Locate every Plasmodium falciparum-infected red blood cell.
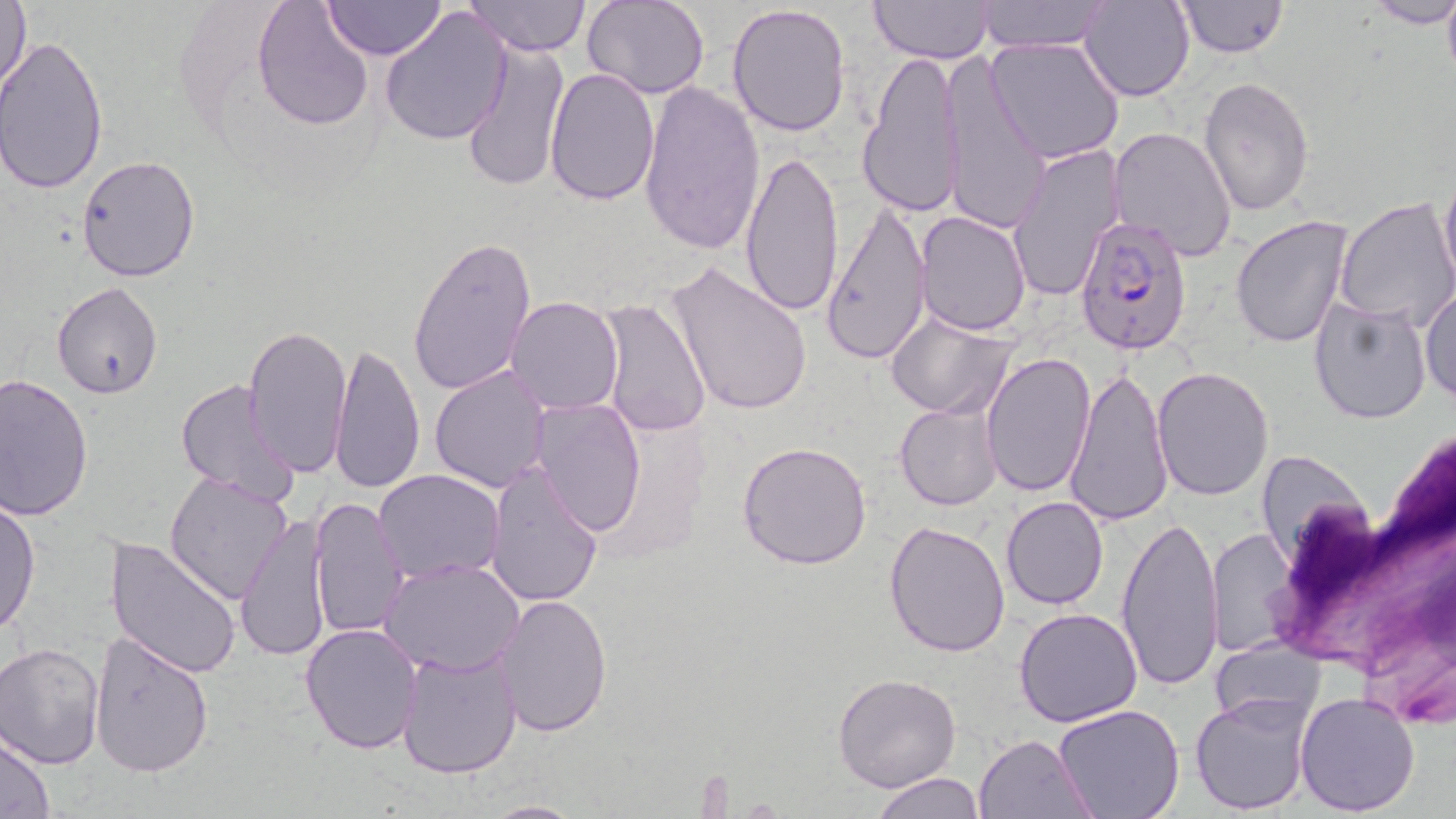
Approximate bounding boxes as (x1, y1, x2, y2) in pixels.
Plasmodium falciparum-infected red blood cells: (1075, 215, 1194, 358).

Summary:
  - Uninfected red blood cell locations: (251, 0, 375, 130), (322, 0, 444, 60), (464, 0, 590, 56), (582, 0, 711, 99), (976, 0, 1114, 52), (1175, 0, 1289, 57), (1, 1, 31, 97), (871, 1, 996, 63), (1080, 1, 1196, 102), (1366, 1, 1456, 29), (379, 4, 513, 145), (725, 4, 853, 135), (0, 35, 108, 196), (986, 37, 1125, 164), (461, 39, 569, 193), (857, 48, 966, 218), (941, 53, 1050, 236), (543, 68, 661, 206), (1198, 76, 1316, 218), (638, 81, 764, 254), (1108, 126, 1238, 264), (1007, 145, 1126, 301), (739, 149, 842, 318), (76, 155, 202, 283), (1439, 172, 1456, 297), (1333, 197, 1456, 330), (819, 205, 934, 363), (916, 212, 1031, 335), (1230, 215, 1354, 349), (407, 233, 537, 398), (664, 263, 812, 417), (52, 282, 165, 399), (1420, 284, 1456, 406), (505, 296, 624, 415), (597, 297, 710, 437), (1307, 297, 1434, 424), (884, 312, 1018, 419), (243, 323, 353, 477), (328, 338, 426, 495), (980, 351, 1096, 499), (1065, 362, 1173, 528), (430, 365, 552, 492), (1151, 367, 1274, 500), (0, 374, 96, 520), (173, 381, 301, 508), (531, 399, 645, 537), (895, 404, 1002, 511), (738, 440, 873, 571), (1258, 449, 1372, 566), (484, 464, 604, 609), (375, 469, 506, 582), (164, 471, 293, 603), (1001, 495, 1110, 611), (0, 497, 40, 638), (308, 498, 411, 638), (1116, 511, 1224, 692), (235, 513, 332, 664), (883, 519, 1012, 657), (1208, 526, 1298, 655), (105, 537, 243, 679), (381, 558, 526, 677), (495, 594, 612, 739), (1013, 608, 1142, 728), (299, 622, 424, 755), (89, 632, 214, 777), (1209, 639, 1325, 732), (0, 641, 104, 769), (396, 644, 524, 779), (833, 673, 962, 791), (1295, 691, 1420, 814), (1190, 692, 1313, 813), (1052, 702, 1186, 819), (975, 733, 1096, 817), (1, 734, 55, 818), (871, 772, 986, 818), (478, 799, 589, 818)
  - Slide-level diagnosis: Plasmodium falciparum
  - Preparation: thin blood film
  - Stain: May-Grünwald-Giemsa
  - Field of view: one of a larger specimen
  - Modality: light microscopy
  - Magnification: 1000x
  - Image size: 1456×819 pixels